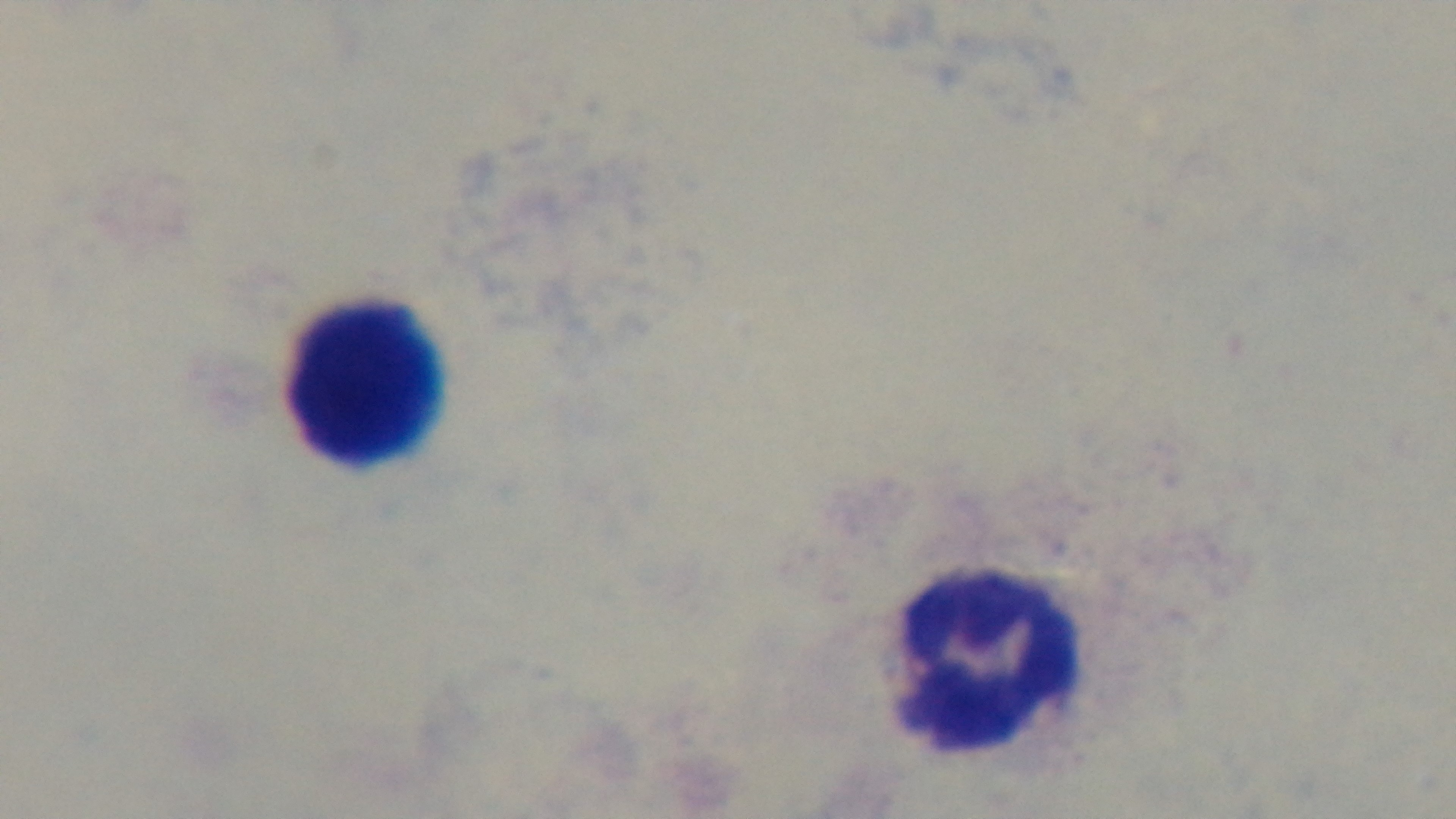
Preparation: thick blood film. Malaria status: negative. Light microscopy. 100x oil-immersion objective. Giemsa-stained. Captured with a mounted 4K digital camera. Single field of view.